Name the blood parasite species.
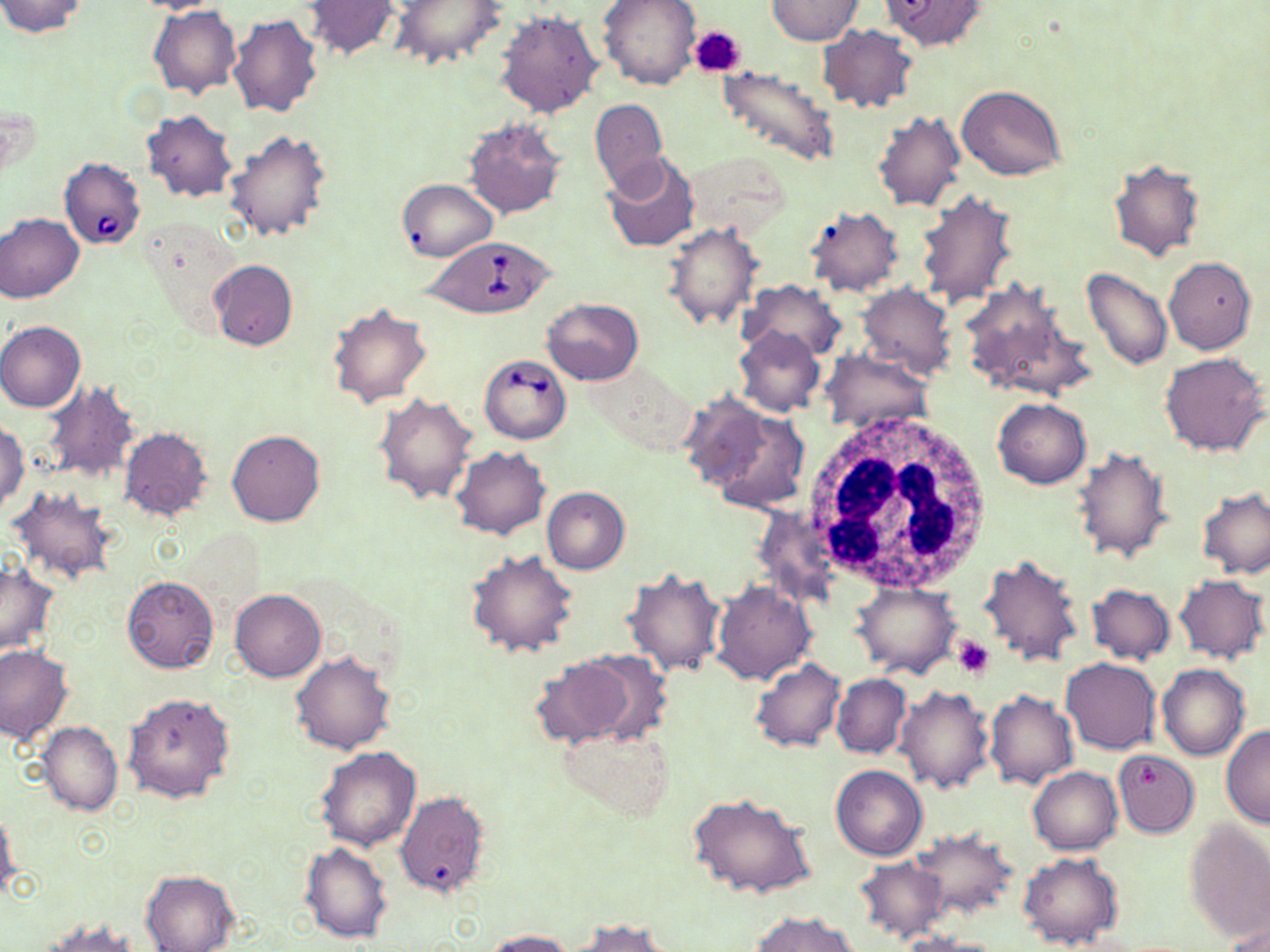

Babesia divergens.

image size = 1270×952 pixels
Babesia divergens-infected red blood cell locations = approximate bounding boxes as (x1,y1)-(x2,y2) corner pairs in pixels: (58,157)-(145,249), (423,237)-(556,318), (479,354)-(571,444)
magnification = 1000x
uninfected red blood cell locations = approximate bounding boxes as (x1,y1)-(x2,y2) corner pairs in pixels: (0,0)-(88,37), (129,0)-(231,15), (303,0)-(401,60), (389,0)-(508,70), (598,0)-(701,91), (767,0)-(863,46), (881,1)-(988,51), (149,7)-(241,98), (495,10)-(604,117), (228,14)-(323,119), (817,23)-(916,114), (717,63)-(840,169), (957,84)-(1066,180), (590,98)-(667,194), (141,110)-(237,201), (872,111)-(966,212), (463,117)-(566,220), (225,128)-(333,241), (601,151)-(698,253), (1107,160)-(1203,262), (398,179)-(497,261), (915,191)-(1019,309), (803,206)-(904,296), (0,213)-(85,304), (662,222)-(764,331), (139,225)-(245,342), (1164,257)-(1256,354), (209,260)-(298,351), (1082,267)-(1172,371), (958,278)-(1093,404), (739,279)-(846,362), (856,282)-(957,380), (542,297)-(643,385), (326,304)-(432,410), (0,321)-(86,412), (735,326)-(826,417), (819,351)-(934,434), (1159,353)-(1268,457), (584,361)-(697,456), (39,380)-(140,484), (374,392)-(478,504), (679,392)-(773,491), (992,398)-(1091,488), (700,405)-(811,511), (0,421)-(30,514), (119,427)-(213,521), (228,430)-(324,528), (1072,445)-(1174,564), (452,447)-(551,540), (8,487)-(119,584), (541,487)-(629,574), (1197,487)-(1270,579), (753,504)-(842,609), (466,548)-(577,658), (978,554)-(1084,670), (1,560)-(58,658), (623,568)-(725,677), (1174,574)-(1269,664), (122,576)-(218,674), (711,580)-(817,687), (852,582)-(962,679), (1086,584)-(1176,665), (231,589)-(326,681), (0,644)-(73,744), (576,650)-(675,747), (291,652)-(395,755), (530,654)-(644,747), (750,658)-(846,753), (1062,658)-(1159,754), (1158,663)-(1249,761), (831,674)-(911,759), (895,685)-(993,792), (984,691)-(1078,790), (123,692)-(236,805), (39,720)-(123,816), (1220,724)-(1270,828), (556,725)-(670,822), (315,745)-(422,851), (1115,750)-(1198,838), (831,766)-(927,861), (1028,767)-(1122,855), (394,791)-(490,899), (689,793)-(816,900), (0,808)-(21,899), (1183,821)-(1270,942), (909,829)-(1018,920), (299,842)-(391,943), (1019,852)-(1124,950), (853,856)-(949,945), (141,871)-(239,951), (750,911)-(857,952), (40,917)-(143,951), (570,919)-(674,952), (1222,924)-(1270,951), (483,930)-(578,952), (896,931)-(1003,952)
stain = May-Grünwald-Giemsa
platelet locations = approximate bounding boxes as (x1,y1)-(x2,y2) corner pairs in pixels: (690,26)-(745,78), (954,637)-(993,679)
field of view = one of a larger specimen
white blood cell locations = approximate bounding boxes as (x1,y1)-(x2,y2) corner pairs in pixels: (806,412)-(997,595)
modality = optical microscopy
preparation = thin blood film